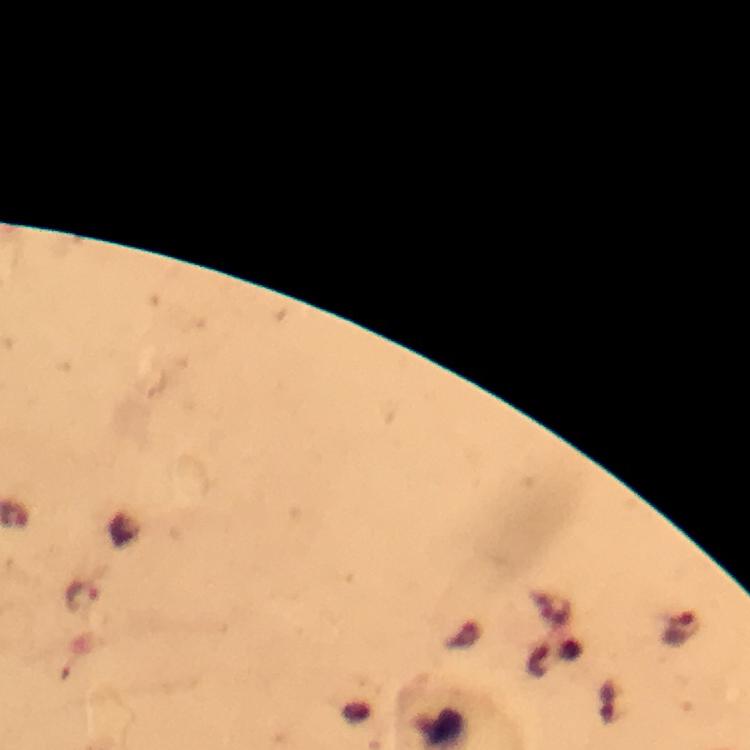

malaria parasite locations = approximate centers as [x, y] in pixels: [83, 596], [681, 630]
image size = 750×750 pixels
immersion oil = applied
magnification = 100x
capture = smartphone camera through the microscope
context = from a malaria diagnostic workup
preparation = thick blood smear
cropped from = one field of view
stain = Giemsa